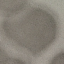
{
  "malaria_status": "uninfected",
  "preparation": "thin blood smear",
  "stain": "Giemsa",
  "capture": "smartphone through the microscope eyepiece",
  "image_type": "cell patch, automatically extracted from a larger field of view and resized to 64 × 64 pixels"
}